Outline each blood parasite and name the species.
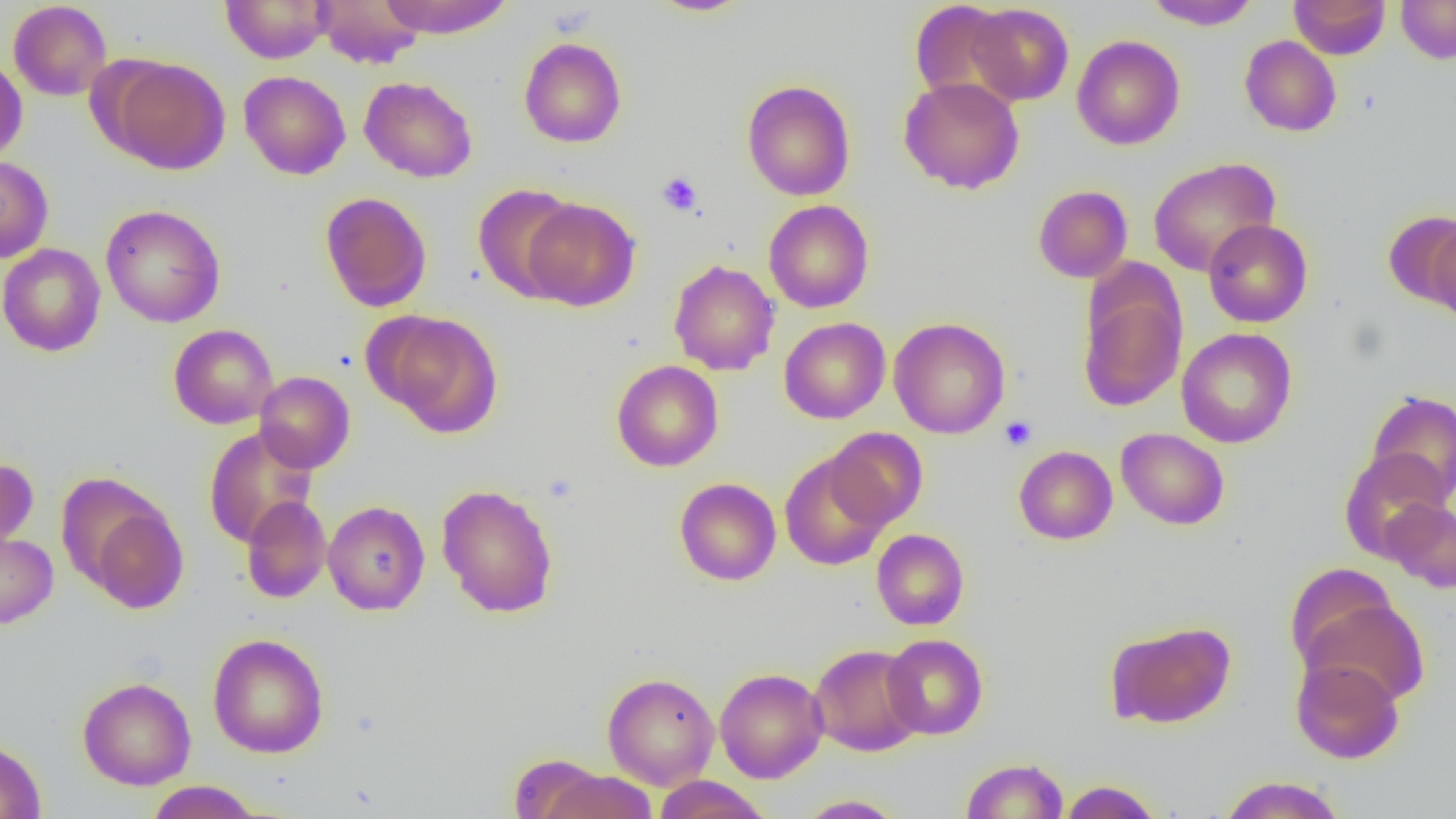
No blood parasites observed.

Summary:
  - Coordinate format: approximate bounding boxes as named x1/y1/x2/y2 corners in pixels
  - Uninfected red blood cell locations: (x1=220, y1=0, x2=333, y2=63), (x1=314, y1=0, x2=424, y2=69), (x1=377, y1=0, x2=514, y2=38), (x1=646, y1=0, x2=755, y2=17), (x1=1144, y1=0, x2=1261, y2=30), (x1=1289, y1=0, x2=1390, y2=59), (x1=1396, y1=0, x2=1456, y2=64), (x1=8, y1=1, x2=112, y2=101), (x1=909, y1=1, x2=1015, y2=104), (x1=965, y1=3, x2=1074, y2=106), (x1=1072, y1=35, x2=1185, y2=150), (x1=1240, y1=35, x2=1341, y2=137), (x1=518, y1=37, x2=627, y2=148), (x1=106, y1=56, x2=231, y2=174), (x1=0, y1=57, x2=27, y2=163), (x1=238, y1=71, x2=351, y2=180), (x1=359, y1=76, x2=478, y2=183), (x1=899, y1=77, x2=1025, y2=194), (x1=741, y1=79, x2=856, y2=201), (x1=0, y1=156, x2=53, y2=263), (x1=1148, y1=157, x2=1281, y2=277), (x1=473, y1=183, x2=580, y2=302), (x1=1033, y1=185, x2=1133, y2=283), (x1=319, y1=191, x2=432, y2=312), (x1=522, y1=198, x2=640, y2=311), (x1=763, y1=200, x2=874, y2=313), (x1=101, y1=204, x2=226, y2=328), (x1=1383, y1=211, x2=1456, y2=309), (x1=1203, y1=219, x2=1313, y2=327), (x1=1427, y1=219, x2=1456, y2=326), (x1=0, y1=243, x2=106, y2=357), (x1=668, y1=259, x2=780, y2=376), (x1=1078, y1=278, x2=1187, y2=412), (x1=372, y1=311, x2=503, y2=436), (x1=779, y1=317, x2=890, y2=424), (x1=889, y1=317, x2=1010, y2=439), (x1=168, y1=324, x2=278, y2=429), (x1=1176, y1=328, x2=1297, y2=448), (x1=611, y1=360, x2=724, y2=471), (x1=254, y1=371, x2=355, y2=473), (x1=1365, y1=390, x2=1456, y2=506), (x1=203, y1=426, x2=319, y2=549), (x1=824, y1=428, x2=928, y2=530), (x1=1116, y1=428, x2=1229, y2=530), (x1=1014, y1=445, x2=1118, y2=544), (x1=1339, y1=449, x2=1450, y2=562), (x1=779, y1=452, x2=891, y2=571), (x1=0, y1=457, x2=38, y2=551), (x1=674, y1=477, x2=781, y2=585), (x1=437, y1=484, x2=558, y2=618), (x1=80, y1=493, x2=189, y2=613), (x1=241, y1=495, x2=331, y2=603), (x1=1382, y1=499, x2=1456, y2=593), (x1=323, y1=501, x2=430, y2=615), (x1=871, y1=528, x2=969, y2=630), (x1=0, y1=531, x2=58, y2=629), (x1=1284, y1=562, x2=1402, y2=674), (x1=1298, y1=591, x2=1429, y2=705), (x1=1105, y1=620, x2=1236, y2=729), (x1=208, y1=633, x2=330, y2=758), (x1=882, y1=634, x2=988, y2=740), (x1=809, y1=644, x2=924, y2=756), (x1=1290, y1=656, x2=1404, y2=764), (x1=715, y1=668, x2=828, y2=783), (x1=602, y1=673, x2=720, y2=789), (x1=77, y1=676, x2=196, y2=790), (x1=0, y1=738, x2=46, y2=818), (x1=510, y1=754, x2=606, y2=817), (x1=961, y1=758, x2=1069, y2=819), (x1=539, y1=769, x2=657, y2=819), (x1=1217, y1=775, x2=1347, y2=819), (x1=652, y1=776, x2=772, y2=819), (x1=1058, y1=779, x2=1164, y2=818), (x1=145, y1=781, x2=264, y2=818), (x1=795, y1=795, x2=907, y2=818)
  - Platelet locations: (x1=656, y1=171, x2=703, y2=216), (x1=999, y1=416, x2=1037, y2=451)
  - Slide-level diagnosis: no evidence of blood parasites
  - Preparation: thin blood film
  - Modality: light microscopy
  - Field of view: single
  - Image size: 1456×819 pixels
  - Magnification: 1000x